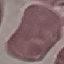
Summary:
  - Malaria status: uninfected
  - Image type: cell patch, automatically extracted from a larger field of view and resized to 64 × 64 pixels
  - Capture: smartphone camera at the microscope eyepiece
  - Preparation: thin blood smear
  - Stain: Giemsa